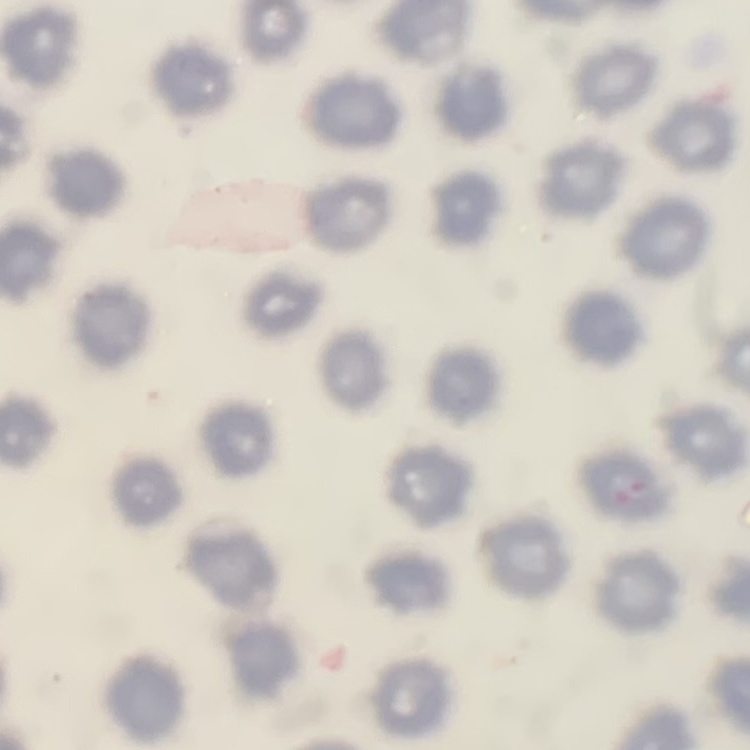 The red blood cells show no rouleaux formation. Thin peripheral smear. Stained with either Field's or Giemsa. One tile cut from a larger photomicrograph.